Assess the morphology of the red blood cells.
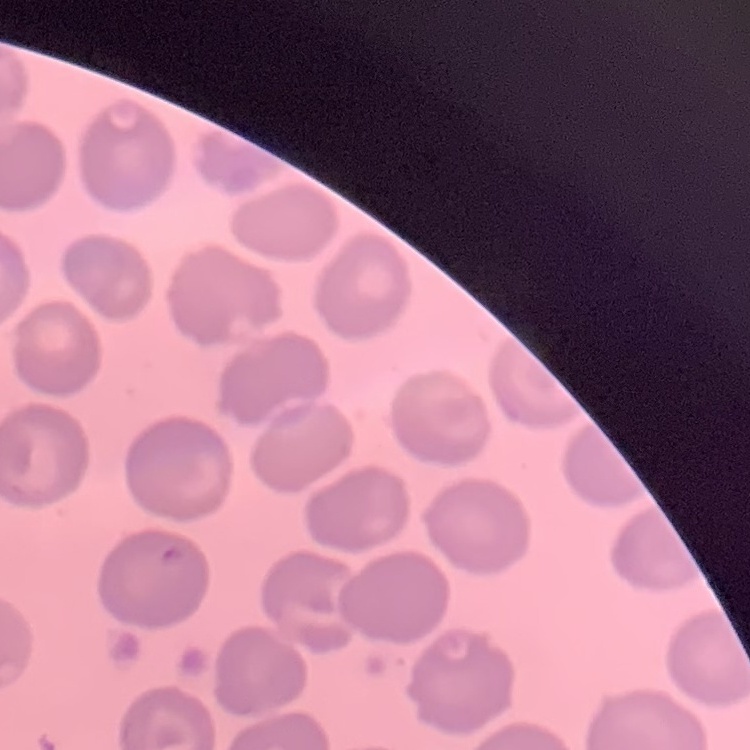
They show no rouleaux formation.

Thin blood film. Field's or Giemsa stain. One tile cut from a larger photomicrograph.